Give the preparation type.
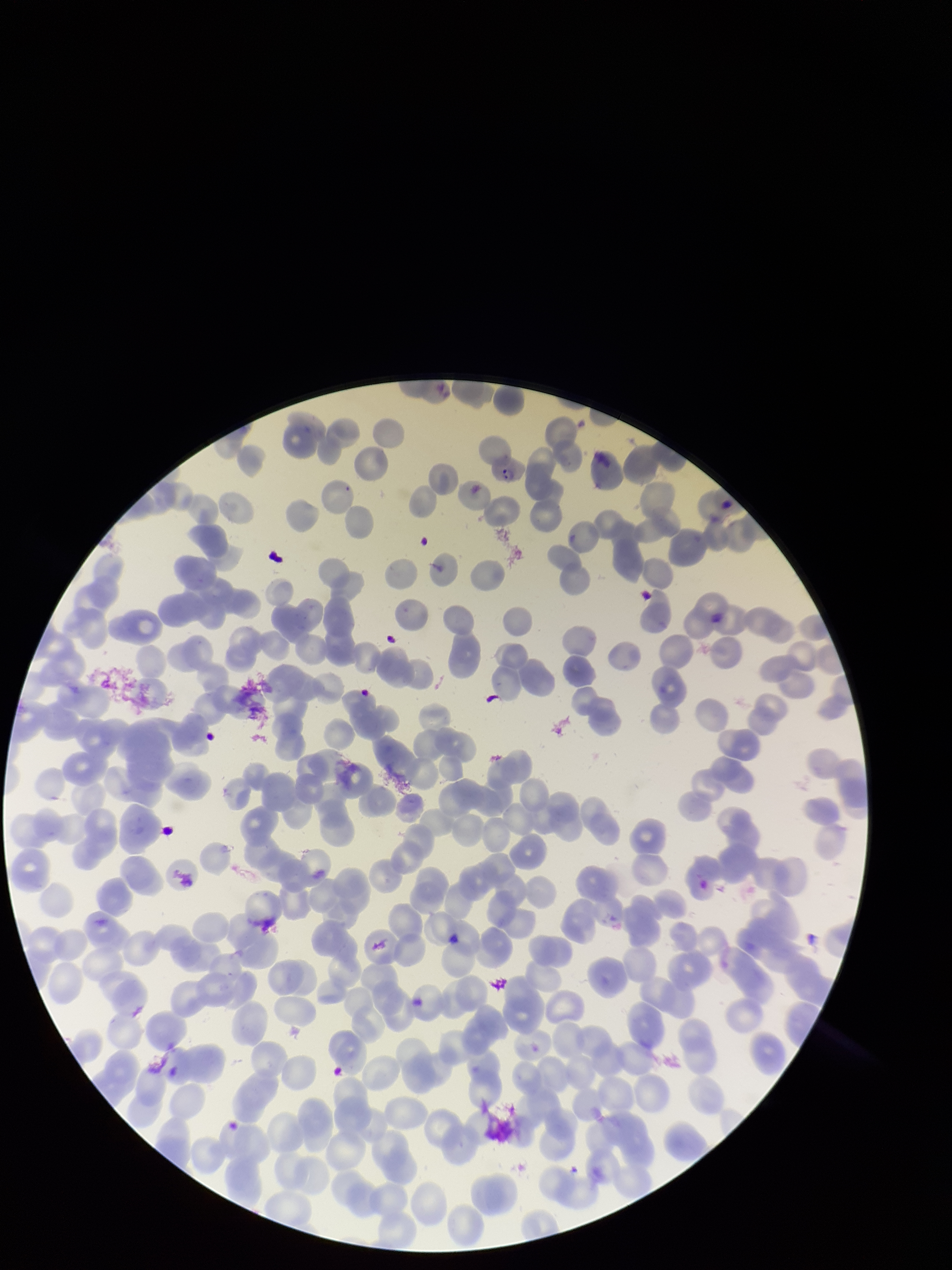
A thin smear.

Image is 952×1270 pixels. Species reported for this patient: Plasmodium falciparum. One field from this slide. Patient malaria status: positive. Parasitized red blood cell count: 1. Giemsa stain. Parasitized red blood cells: identified. Photographed through the microscope eyepiece with a smartphone camera. Red blood cell count: 202.